Give the position of every Plasmodium parasite and every leukocyte.
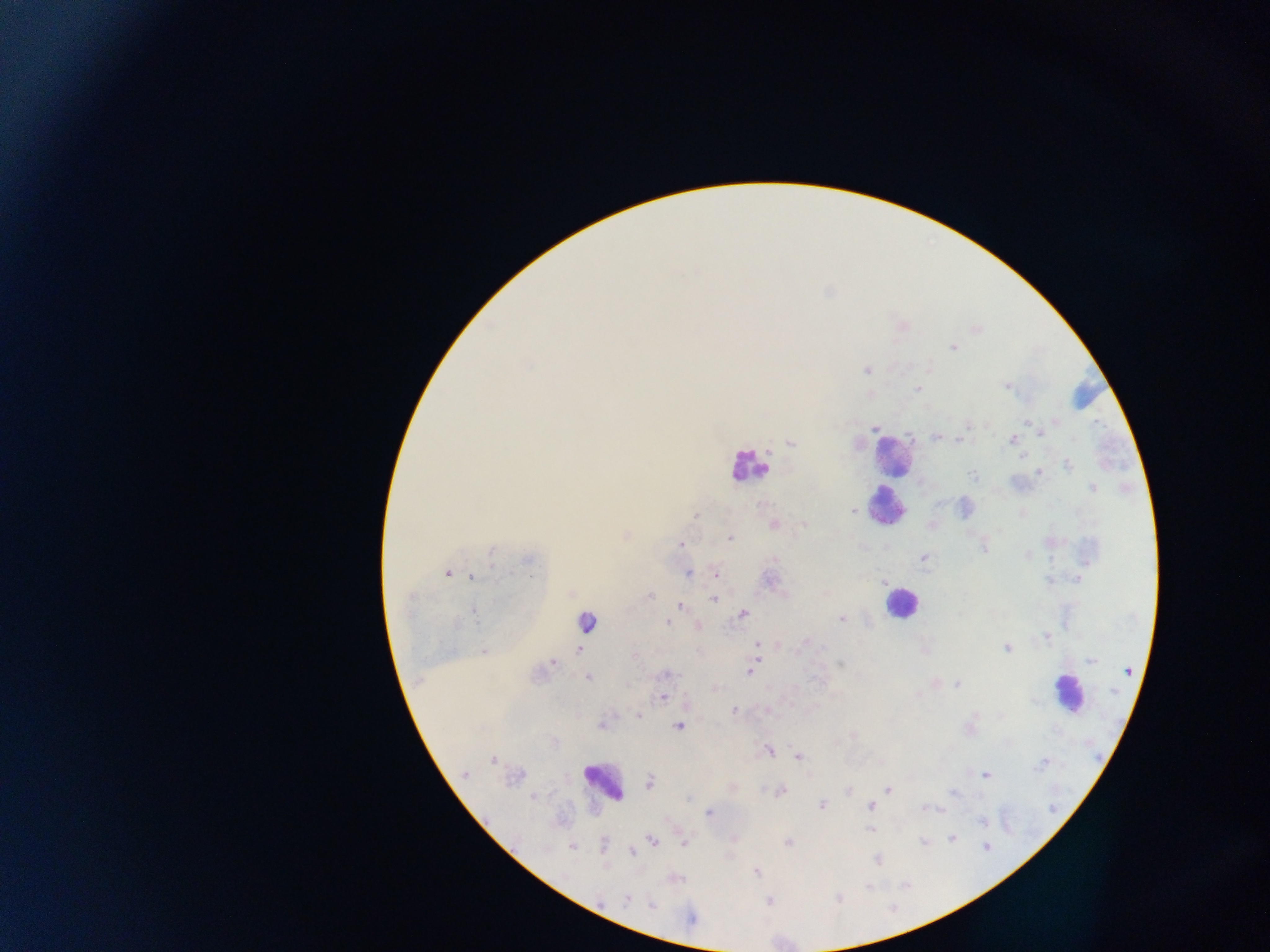

Approximate centers as [x, y] in pixels.
Plasmodium parasites: [953, 348], [529, 366], [867, 370], [1007, 386], [917, 389], [1055, 422], [1028, 423], [968, 426], [875, 427], [1039, 431], [936, 437], [960, 440], [1011, 440], [790, 444], [1022, 458], [1068, 466], [1040, 472], [972, 475], [1092, 488], [853, 511], [696, 515], [774, 524], [804, 525], [730, 538], [682, 545], [983, 549], [491, 552], [1027, 555], [924, 557], [775, 559], [529, 560], [447, 573], [688, 573], [716, 573], [530, 575], [472, 577], [1078, 579], [769, 580], [1048, 581], [884, 582], [649, 596], [714, 599], [680, 605], [474, 612], [743, 613], [841, 619], [456, 623], [668, 623], [698, 626], [1046, 636], [756, 644], [804, 644], [1006, 648], [579, 649], [484, 651], [634, 656], [757, 660], [1091, 660], [553, 663], [840, 664], [750, 667], [1128, 671], [750, 672], [666, 674], [588, 678], [957, 684], [715, 688], [1114, 692], [663, 697], [734, 712], [638, 716], [601, 725], [679, 727], [853, 736], [554, 743], [769, 750], [798, 757], [493, 760], [1042, 763], [465, 774], [985, 775], [649, 783], [888, 790], [848, 791], [780, 792], [954, 793], [535, 797], [688, 798], [822, 805], [870, 806], [924, 808], [941, 809], [709, 813], [983, 821], [870, 829], [952, 837], [653, 841], [788, 842], [923, 842], [684, 844], [603, 846], [986, 846], [571, 847], [632, 852], [876, 860], [757, 872], [868, 887], [627, 899], [838, 899], [652, 905], [691, 919].
Leukocytes: [1084, 398], [891, 454], [748, 467], [887, 506], [901, 602], [586, 618], [1066, 693], [603, 781].

Summary:
  - Capture: mobile-phone photograph through a microscope
  - Field of view: single
  - Country: Ghana
  - Image size: 1270×952 pixels
  - Preparation: thick blood smear